Assess this cell for malaria.
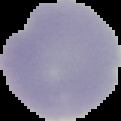

Uninfected.

Summary:
  - Image type: segmented cell region on a black background
  - Preparation: thin blood smear
  - Image size: 121×121 pixels